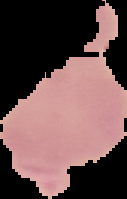

Cell region segmented out of the field of view; the surrounding area is masked to black. From a thin blood film. Malaria status: parasitized. Image is 127×199 pixels.